Report the malaria status of this cell.
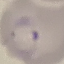

It is parasitized.

Thin blood film. Automatically extracted cell patch, resized to 64 × 64 pixels. Photographed with a smartphone camera at the microscope eyepiece. Giemsa-stained preparation.